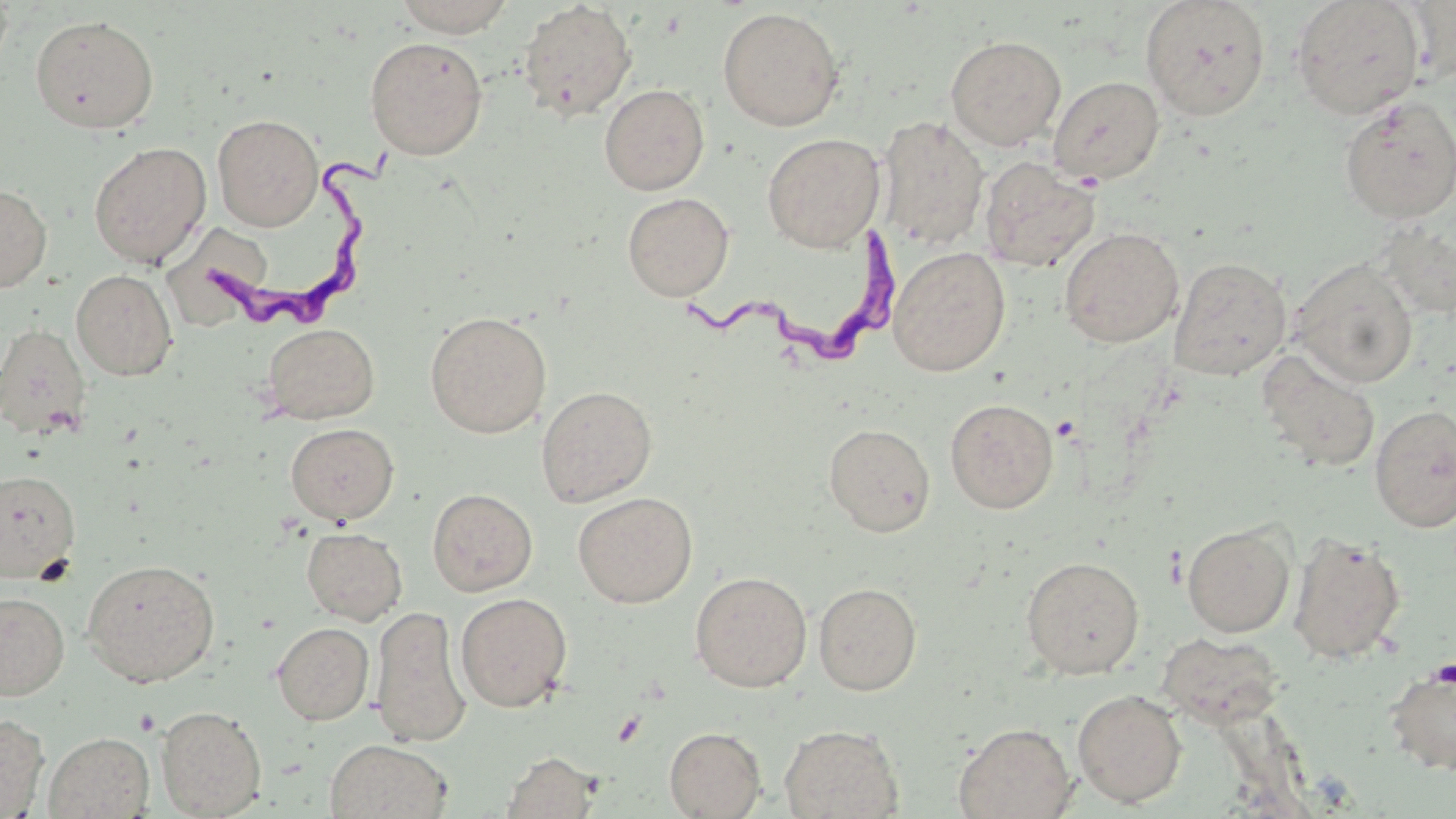
slide-level diagnosis = Trypanosoma brucei
platelet locations = approximate bounding boxes as (x1,y1)-(x2,y2) corner pairs in pixels: (1430,659)-(1456,688)
modality = light microscopy
field of view = one of a larger specimen
image size = 1456×819 pixels
stain = May-Grünwald-Giemsa
magnification = 1000x
preparation = thin blood smear
uninfected red blood cell locations = approximate bounding boxes as (x1,y1)-(x2,y2) corner pairs in pixels: (392,0)-(517,35), (1140,0)-(1270,121), (1291,0)-(1425,119), (1402,0)-(1456,85), (517,1)-(637,120), (717,7)-(845,131), (30,14)-(159,134), (945,35)-(1067,150), (364,36)-(488,159), (1048,75)-(1165,185), (599,84)-(710,194), (1338,95)-(1456,223), (212,114)-(323,230), (877,116)-(989,249), (762,133)-(885,252), (88,141)-(212,268), (980,156)-(1100,272), (0,183)-(52,293), (622,192)-(734,301), (1374,219)-(1456,320), (1059,226)-(1185,348), (177,227)-(284,335), (888,246)-(1011,377), (1169,256)-(1292,380), (1289,257)-(1419,388), (71,269)-(178,380), (424,311)-(552,438), (0,323)-(92,441), (261,323)-(380,424), (1257,350)-(1381,472), (536,386)-(657,507), (945,398)-(1059,514), (1370,404)-(1456,532), (285,423)-(399,524), (823,423)-(935,536), (0,469)-(81,583), (427,488)-(538,596), (572,491)-(697,608), (1182,521)-(1296,637), (301,527)-(407,625), (1288,531)-(1407,665), (1021,556)-(1145,679), (81,558)-(220,687), (690,571)-(812,692), (813,582)-(922,695), (1,591)-(70,700), (455,592)-(573,711), (371,606)-(472,747), (272,622)-(374,725), (1156,632)-(1285,729), (1385,665)-(1456,776), (1073,688)-(1187,808), (155,705)-(267,818), (0,714)-(48,818), (952,722)-(1077,819), (779,724)-(904,819), (664,727)-(765,818), (44,732)-(154,818), (325,739)-(451,819), (500,751)-(601,819)
Trypanosoma brucei locations = approximate bounding boxes as (x1,y1)-(x2,y2) corner pairs in pixels: (203,140)-(404,336), (681,222)-(908,370)